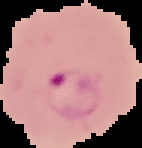
Malaria status: parasitized. Image is 142×148 pixels. Cell region segmented out of the field of view; the surrounding area is masked to black. From a thin blood smear.